Outline each uninfected red blood cell.
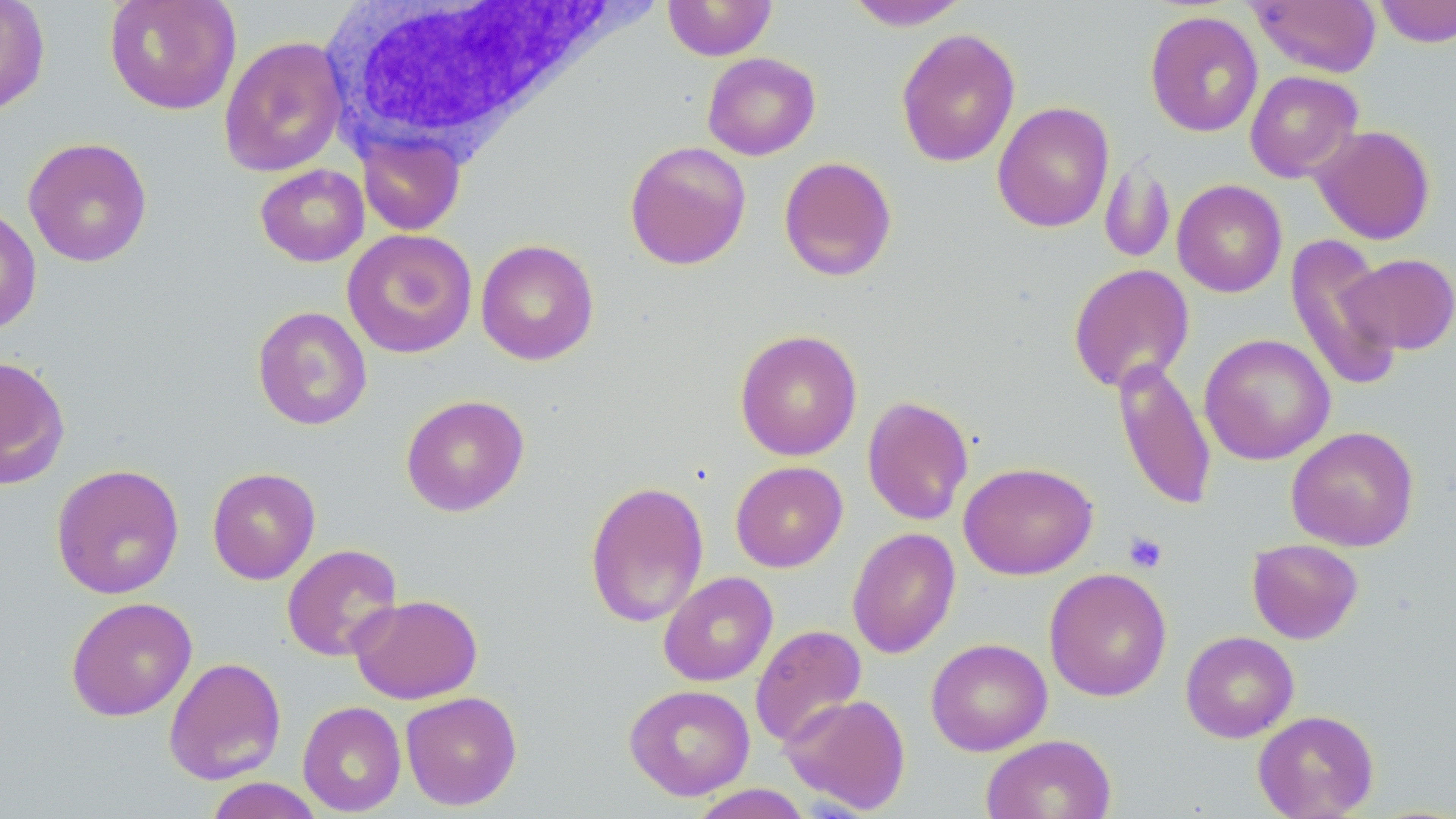

Approximate bounding boxes as (x1, y1, x2, y2) in pixels.
Uninfected red blood cells: (0, 0, 50, 116), (103, 0, 241, 115), (844, 0, 972, 30), (1374, 0, 1456, 48), (663, 1, 778, 60), (1248, 1, 1382, 77), (1144, 10, 1264, 138), (896, 28, 1021, 168), (218, 35, 349, 177), (702, 52, 820, 160), (1245, 70, 1363, 182), (992, 101, 1114, 233), (1311, 125, 1435, 245), (357, 130, 466, 236), (22, 137, 153, 268), (624, 140, 751, 271), (778, 156, 897, 281), (1099, 158, 1176, 264), (255, 163, 370, 267), (1172, 179, 1287, 297), (0, 204, 42, 335), (342, 229, 478, 359), (1285, 234, 1403, 394), (476, 239, 599, 365), (1344, 253, 1456, 355), (1068, 263, 1195, 394), (252, 306, 373, 431), (734, 329, 862, 461), (1199, 333, 1336, 465), (0, 354, 70, 489), (1112, 357, 1218, 513), (400, 394, 530, 517), (861, 395, 975, 526), (1286, 426, 1420, 552), (730, 460, 848, 572), (959, 462, 1098, 579), (50, 463, 184, 600), (206, 467, 321, 585), (584, 480, 709, 628), (847, 527, 960, 659), (1247, 538, 1364, 644), (282, 543, 403, 661), (1044, 567, 1172, 702), (658, 571, 778, 687), (349, 594, 483, 705), (65, 596, 197, 721), (749, 623, 867, 749), (1180, 630, 1299, 743), (926, 637, 1052, 756), (163, 656, 287, 785), (624, 683, 755, 801), (401, 691, 522, 810), (781, 693, 911, 814), (297, 701, 406, 816), (1252, 709, 1379, 818), (981, 734, 1117, 819), (204, 777, 326, 818), (688, 784, 813, 818).

slide-level diagnosis = no evidence of blood parasites
platelet locations = approximate bounding boxes as (x1, y1, x2, y2) in pixels: (1122, 531, 1168, 574)
white blood cell locations = approximate bounding boxes as (x1, y1, x2, y2) in pixels: (320, 3, 618, 158)
magnification = 1000x
image size = 1456×819 pixels
stain = May-Grünwald-Giemsa
preparation = thin blood film
modality = optical microscopy
field of view = one of a larger specimen